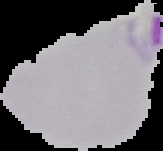
From a thin blood smear. Malaria status: parasitized. Image is 163×151 pixels. Cell region segmented out of the field of view; the surrounding area is masked to black.